Classify this cell by malaria status.
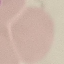

Uninfected.

Thin blood film. Automatically extracted cell patch, resized to 64 × 64 pixels. Giemsa-stained preparation. Photographed with a smartphone camera at the microscope eyepiece.